Give the preparation type.
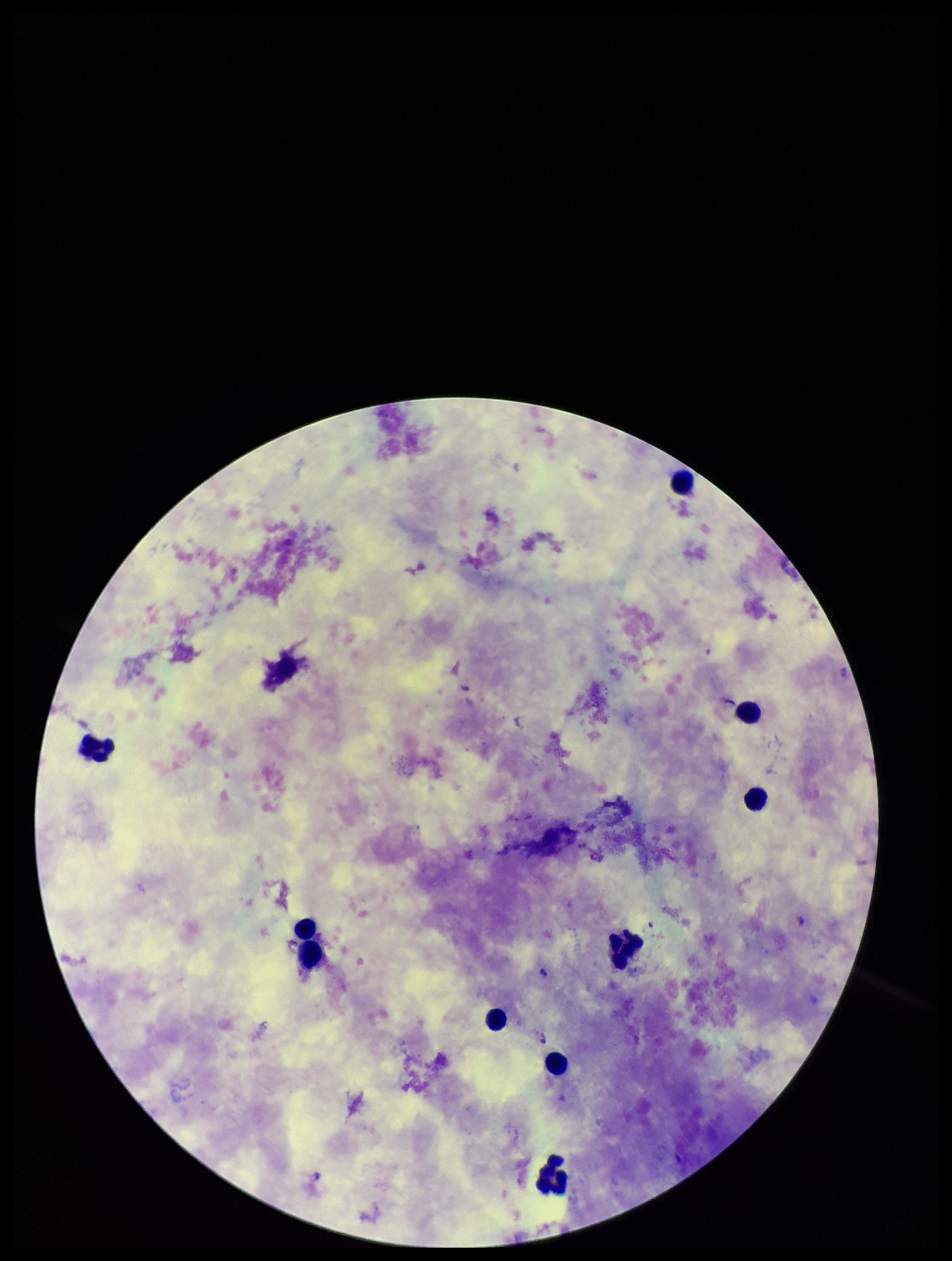
It is a thick blood smear.

Summary:
  - Stain: Giemsa
  - Leukocyte count: 10
  - Capture: smartphone photograph through the microscope eyepiece
  - Field of view: one from this slide
  - Patient malaria status: positive
  - Plasmodium parasites: seen
  - Image size: 952×1261 pixels
  - Species reported for this patient: Plasmodium falciparum
  - Parasite count: 1